Assess the morphology of the erythrocytes.
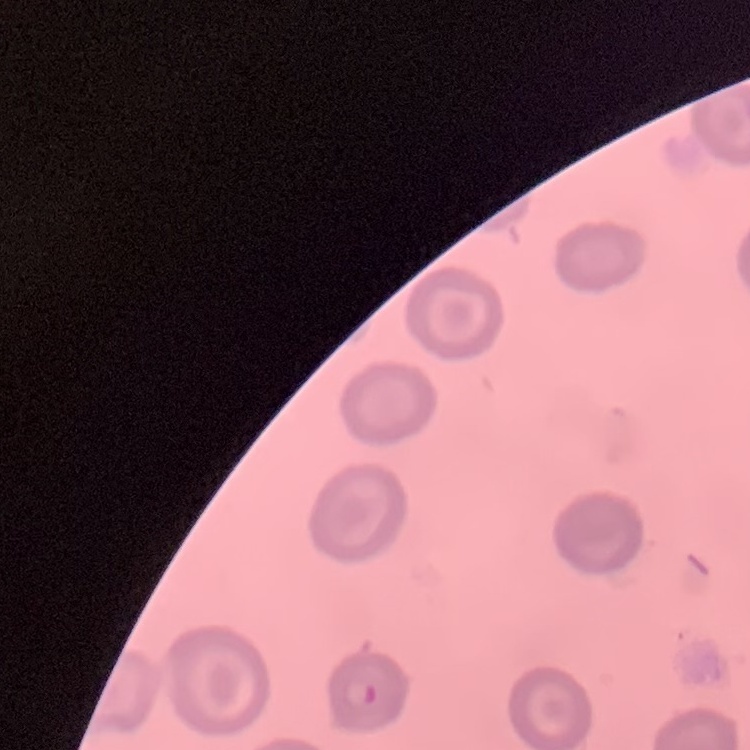

No rouleaux formation.

{
  "preparation": "thin blood smear",
  "image_type": "square crop of a larger photomicrograph",
  "stain": "Field's or Giemsa"
}